Comment on the morphology of the erythrocytes.
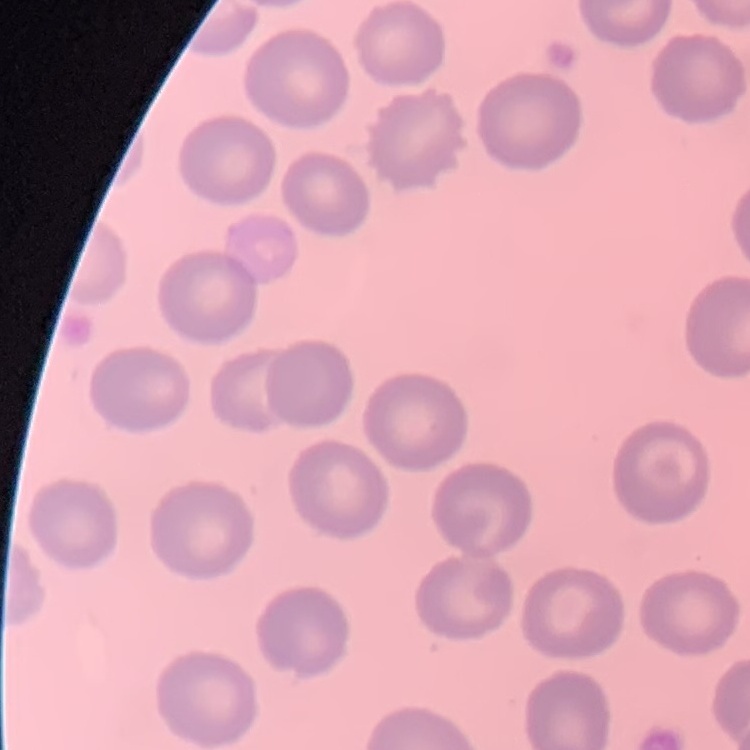

No rouleaux formation.

Summary:
  - Stain: Field's or Giemsa
  - Image type: one tile cut from a larger photomicrograph
  - Preparation: thin blood film